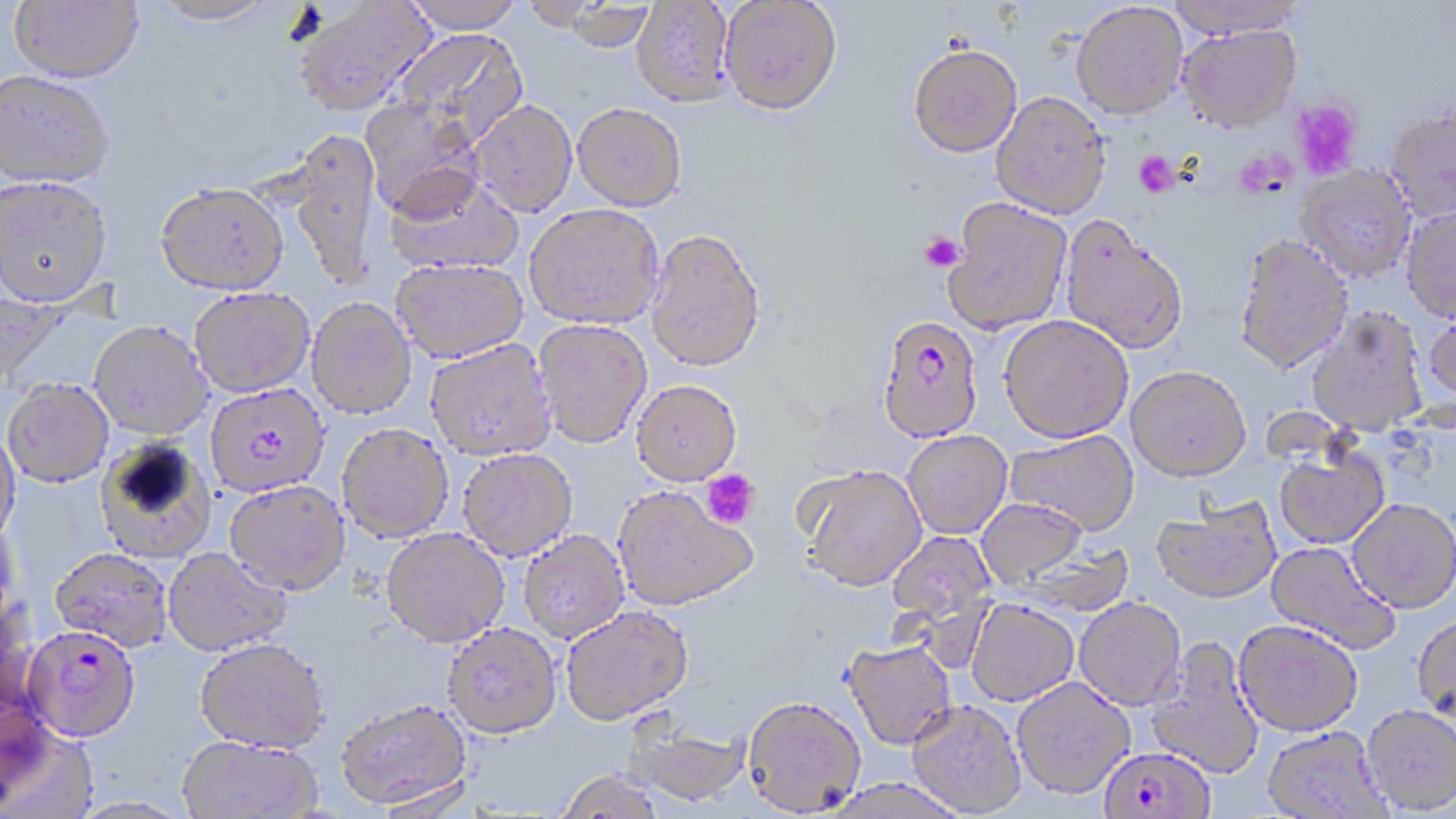

slide-level diagnosis = Plasmodium falciparum
magnification = 1000x
modality = optical microscopy
uninfected red blood cell locations = approximate bounding boxes as named x1/y1/x2/y2 corners in pixels: (x1=9, y1=0, x2=144, y2=85), (x1=152, y1=0, x2=277, y2=27), (x1=293, y1=0, x2=433, y2=117), (x1=402, y1=0, x2=526, y2=33), (x1=517, y1=0, x2=617, y2=28), (x1=1165, y1=0, x2=1305, y2=38), (x1=632, y1=1, x2=735, y2=106), (x1=720, y1=1, x2=843, y2=114), (x1=551, y1=2, x2=657, y2=50), (x1=1072, y1=2, x2=1187, y2=120), (x1=1178, y1=24, x2=1301, y2=131), (x1=388, y1=28, x2=528, y2=148), (x1=908, y1=44, x2=1022, y2=157), (x1=0, y1=70, x2=115, y2=189), (x1=992, y1=91, x2=1110, y2=218), (x1=361, y1=98, x2=487, y2=220), (x1=470, y1=99, x2=577, y2=217), (x1=573, y1=102, x2=687, y2=211), (x1=1385, y1=106, x2=1456, y2=220), (x1=287, y1=131, x2=382, y2=289), (x1=1296, y1=164, x2=1415, y2=281), (x1=386, y1=172, x2=524, y2=276), (x1=0, y1=177, x2=113, y2=309), (x1=154, y1=182, x2=289, y2=295), (x1=944, y1=198, x2=1071, y2=334), (x1=525, y1=203, x2=664, y2=329), (x1=1400, y1=205, x2=1456, y2=320), (x1=1060, y1=215, x2=1188, y2=355), (x1=646, y1=228, x2=766, y2=372), (x1=1234, y1=233, x2=1353, y2=374), (x1=391, y1=258, x2=528, y2=363), (x1=0, y1=287, x2=64, y2=394), (x1=189, y1=288, x2=315, y2=398), (x1=306, y1=299, x2=417, y2=420), (x1=1307, y1=307, x2=1428, y2=436), (x1=1424, y1=308, x2=1456, y2=409), (x1=999, y1=315, x2=1133, y2=442), (x1=532, y1=319, x2=653, y2=449), (x1=88, y1=322, x2=213, y2=442), (x1=425, y1=340, x2=557, y2=463), (x1=1126, y1=365, x2=1250, y2=482), (x1=631, y1=380, x2=742, y2=487), (x1=3, y1=381, x2=114, y2=490), (x1=336, y1=425, x2=454, y2=544), (x1=1005, y1=428, x2=1139, y2=535), (x1=0, y1=429, x2=22, y2=547), (x1=902, y1=430, x2=1012, y2=538), (x1=96, y1=437, x2=218, y2=565), (x1=458, y1=449, x2=578, y2=562), (x1=1274, y1=449, x2=1389, y2=549), (x1=798, y1=465, x2=927, y2=593), (x1=225, y1=482, x2=350, y2=599), (x1=613, y1=488, x2=758, y2=613), (x1=976, y1=498, x2=1088, y2=587), (x1=1347, y1=498, x2=1456, y2=613), (x1=1151, y1=499, x2=1280, y2=604), (x1=0, y1=517, x2=20, y2=634), (x1=381, y1=529, x2=509, y2=650), (x1=886, y1=530, x2=997, y2=643), (x1=519, y1=531, x2=629, y2=645), (x1=1266, y1=540, x2=1401, y2=655), (x1=1006, y1=542, x2=1137, y2=616), (x1=49, y1=549, x2=172, y2=654), (x1=162, y1=549, x2=292, y2=658), (x1=1075, y1=596, x2=1187, y2=710), (x1=0, y1=599, x2=41, y2=725), (x1=966, y1=599, x2=1078, y2=706), (x1=560, y1=606, x2=694, y2=728), (x1=1413, y1=614, x2=1456, y2=724), (x1=1233, y1=619, x2=1363, y2=736), (x1=442, y1=625, x2=563, y2=743), (x1=1146, y1=634, x2=1265, y2=780), (x1=842, y1=640, x2=957, y2=751), (x1=194, y1=641, x2=329, y2=757), (x1=1012, y1=676, x2=1135, y2=798), (x1=742, y1=696, x2=865, y2=817), (x1=336, y1=701, x2=474, y2=813), (x1=906, y1=701, x2=1026, y2=816), (x1=1361, y1=704, x2=1456, y2=814), (x1=624, y1=716, x2=751, y2=808), (x1=0, y1=719, x2=96, y2=819), (x1=1263, y1=726, x2=1391, y2=819), (x1=177, y1=738, x2=322, y2=818), (x1=556, y1=771, x2=665, y2=818), (x1=823, y1=779, x2=971, y2=819), (x1=69, y1=798, x2=199, y2=819)
field of view = single
platelet locations = approximate bounding boxes as named x1/y1/x2/y2 corners in pixels: (x1=1290, y1=99, x2=1362, y2=180), (x1=1133, y1=151, x2=1180, y2=198), (x1=919, y1=231, x2=965, y2=273), (x1=700, y1=468, x2=761, y2=530)
preparation = thin blood film
image size = 1456×819 pixels
stain = May-Grünwald-Giemsa
Plasmodium falciparum-infected red blood cell locations = approximate bounding boxes as named x1/y1/x2/y2 corners in pixels: (x1=878, y1=314, x2=984, y2=444), (x1=205, y1=384, x2=330, y2=499), (x1=21, y1=628, x2=142, y2=745), (x1=1094, y1=749, x2=1223, y2=819)